Draw a bounding box around every malaria parasite, every leukocyte, and every artifact (stain precipitate or debris).
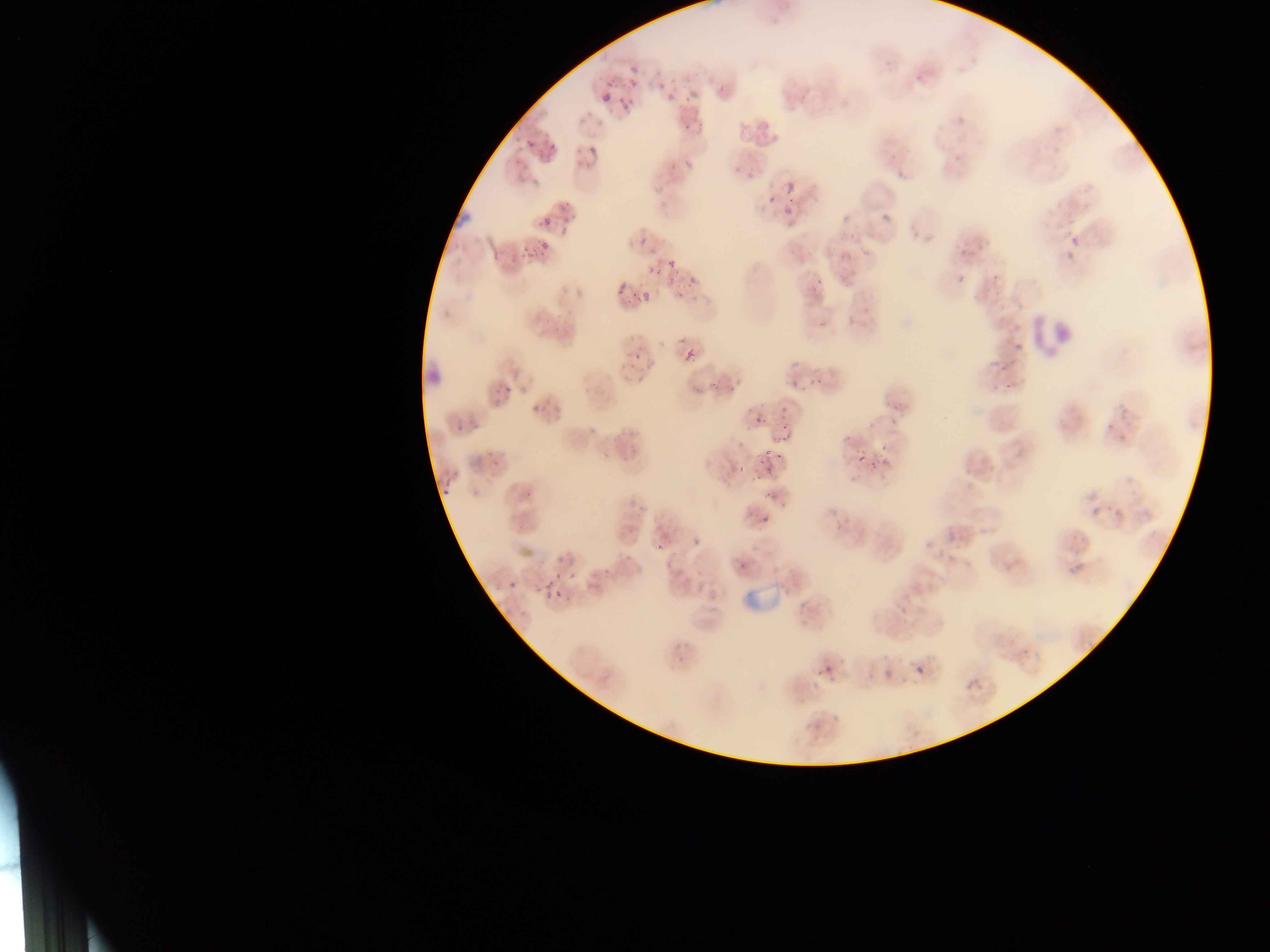
Approximate bounding boxes as {left, top, right, bottom} in pixels.
Malaria parasites: {631, 66, 637, 75}, {671, 78, 676, 86}, {607, 80, 616, 87}, {601, 89, 613, 102}, {668, 90, 676, 102}, {683, 94, 693, 102}, {622, 104, 631, 112}, {685, 122, 693, 132}, {550, 137, 557, 150}, {527, 138, 534, 146}, {590, 144, 598, 157}, {683, 157, 693, 169}, {736, 163, 740, 174}, {786, 181, 798, 196}, {767, 196, 775, 202}, {565, 200, 572, 210}, {783, 206, 793, 213}, {881, 209, 892, 225}, {544, 215, 552, 228}, {850, 230, 855, 238}, {639, 236, 649, 245}, {1071, 236, 1080, 243}, {542, 238, 551, 253}, {523, 246, 531, 252}, {1067, 253, 1075, 260}, {668, 259, 675, 267}, {649, 267, 654, 275}, {656, 271, 664, 276}, {691, 275, 697, 285}, {816, 275, 824, 283}, {959, 275, 967, 284}, {669, 278, 674, 286}, {617, 285, 625, 295}, {643, 292, 648, 300}, {680, 292, 685, 300}, {820, 320, 825, 330}, {684, 346, 695, 362}, {635, 352, 640, 360}, {817, 377, 823, 386}, {793, 379, 798, 389}, {506, 381, 511, 389}, {710, 381, 717, 389}, {1005, 383, 1013, 391}, {534, 403, 538, 413}, {553, 404, 562, 411}, {781, 407, 789, 412}, {755, 416, 761, 424}, {587, 423, 595, 434}, {786, 432, 794, 442}, {842, 434, 853, 440}, {879, 444, 889, 453}, {775, 453, 783, 461}, {858, 457, 867, 464}, {882, 457, 892, 465}, {869, 462, 878, 468}, {758, 476, 766, 482}, {442, 486, 451, 497}, {1093, 506, 1098, 515}, {762, 516, 770, 522}, {693, 538, 698, 546}, {658, 543, 663, 551}, {667, 558, 676, 567}, {1077, 562, 1084, 570}, {570, 570, 580, 579}, {554, 573, 562, 581}, {545, 578, 554, 589}, {507, 579, 519, 588}, {555, 590, 565, 595}, {546, 591, 553, 603}, {900, 609, 912, 615}, {826, 664, 834, 673}, {816, 667, 824, 678}, {917, 667, 925, 677}, {884, 670, 891, 681}, {865, 674, 874, 680}, {831, 712, 841, 722}, {805, 723, 812, 732} | approximate {x, y} pixel centers of objects too small to bound: {658, 72}, {635, 84}, {663, 86}, {622, 100}, {532, 255}, {635, 295}, {630, 307}, {682, 340}, {811, 383}, {731, 389}, {498, 391}, {543, 407}, {459, 427}, {785, 427}, {1110, 427}, {1120, 436}, {768, 451}, {490, 453}, {606, 454}, {497, 463}, {740, 470}, {529, 495}, {768, 496}, {629, 558}, {606, 571}, {539, 590}, {687, 644}, {681, 661}.
Leukocytes: {451, 204, 477, 228}, {1030, 306, 1075, 358}, {425, 358, 447, 388}.
Artifacts (stain precipitate or debris): {735, 583, 784, 619}.

Summary:
  - Field of view: single
  - Capture: mobile-phone photograph through a microscope
  - Preparation: thin blood film
  - Country: Ghana
  - Image size: 1270×952 pixels